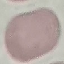

Summary:
  - Result: no malaria parasites seen
  - Preparation: thin blood smear
  - Stain: Giemsa
  - Capture: smartphone camera at the microscope eyepiece
  - Image type: cell patch, automatically extracted from a larger field of view and resized to 64 × 64 pixels